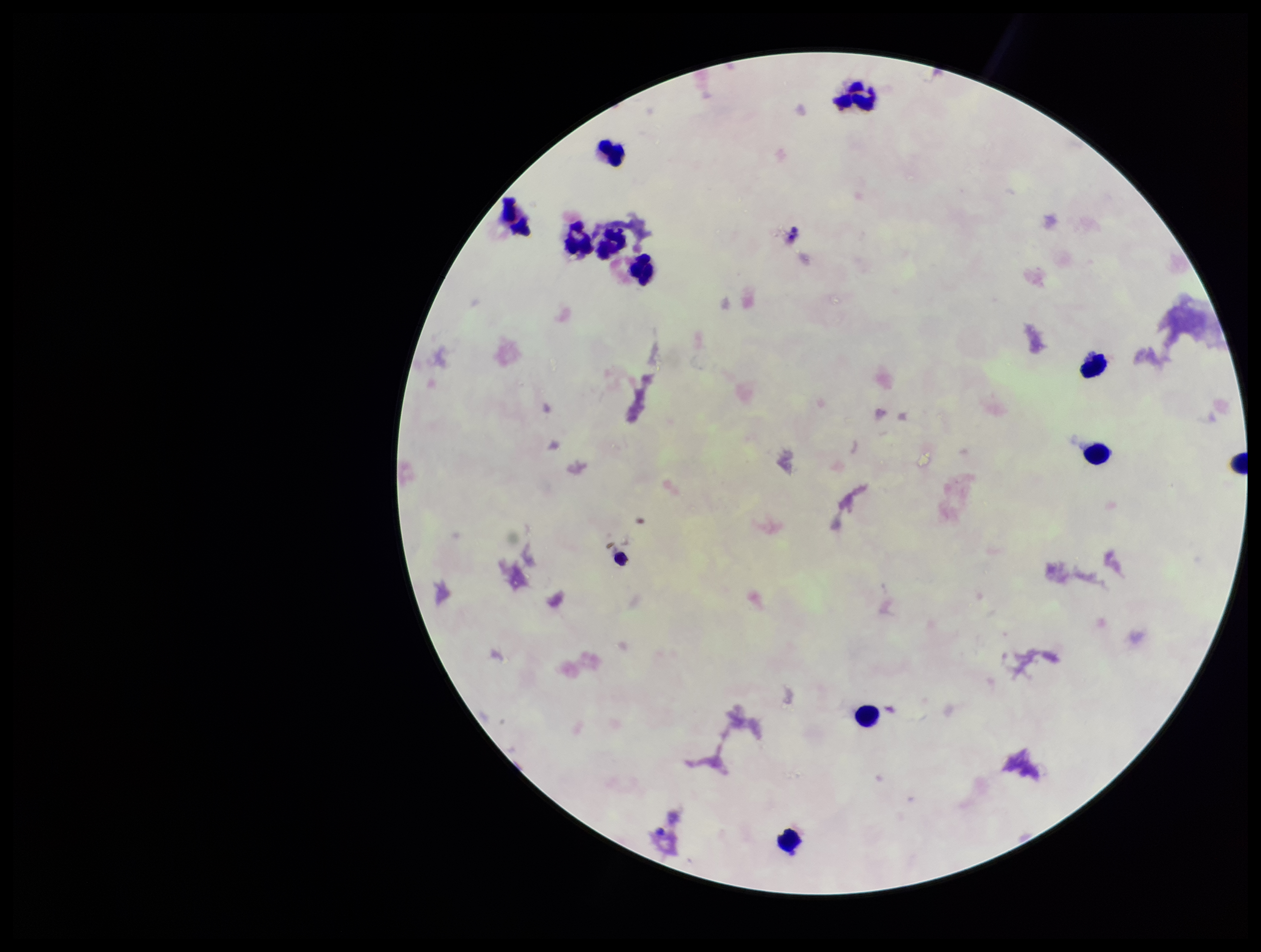
Summary:
  - Patient malaria status: negative
  - Preparation: thick blood smear
  - Parasite count: 0
  - Plasmodium parasites: none identified
  - Capture: smartphone photograph through the microscope eyepiece
  - Field of view: single
  - Image size: 1261×952 pixels
  - Stain: Giemsa
  - Leukocyte count: 11